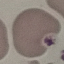 Malaria status: uninfected. Giemsa-stained preparation. Cell patch, automatically extracted from a larger field of view and resized to 64 × 64 pixels. Acquired by smartphone through the microscope eyepiece. Thin blood film.